Name the parasite shown.
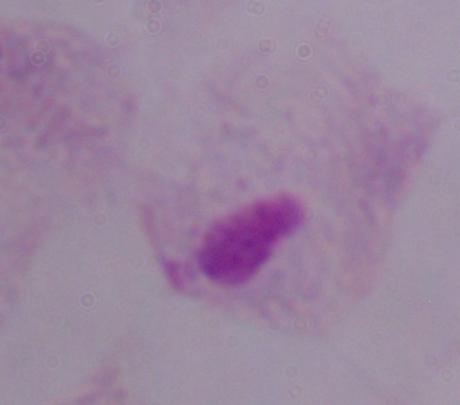

This is a trichomonad.

Summary:
  - Modality: micrograph
  - Magnification: 1000x